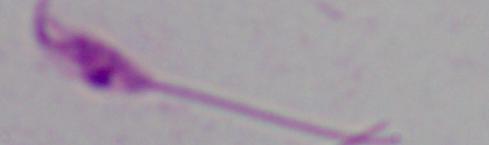 Captured at 1000x magnification. Photomicrograph. A Leishmania parasite is seen.